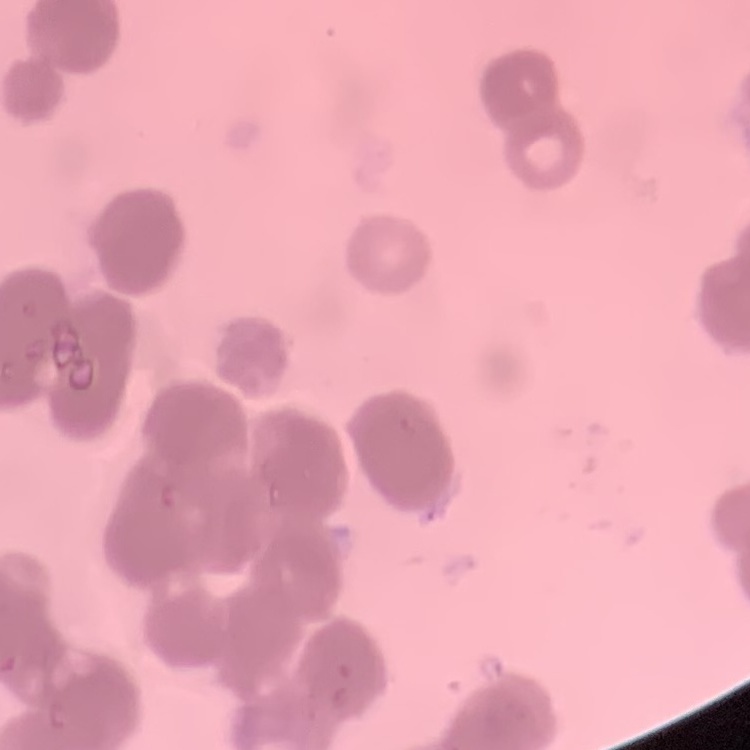
{
  "red_blood_cell_morphology": "rouleaux formation",
  "stain": "Field's or Giemsa",
  "image_type": "square crop of a larger photomicrograph",
  "preparation": "thin blood film"
}